Identify the preparation type.
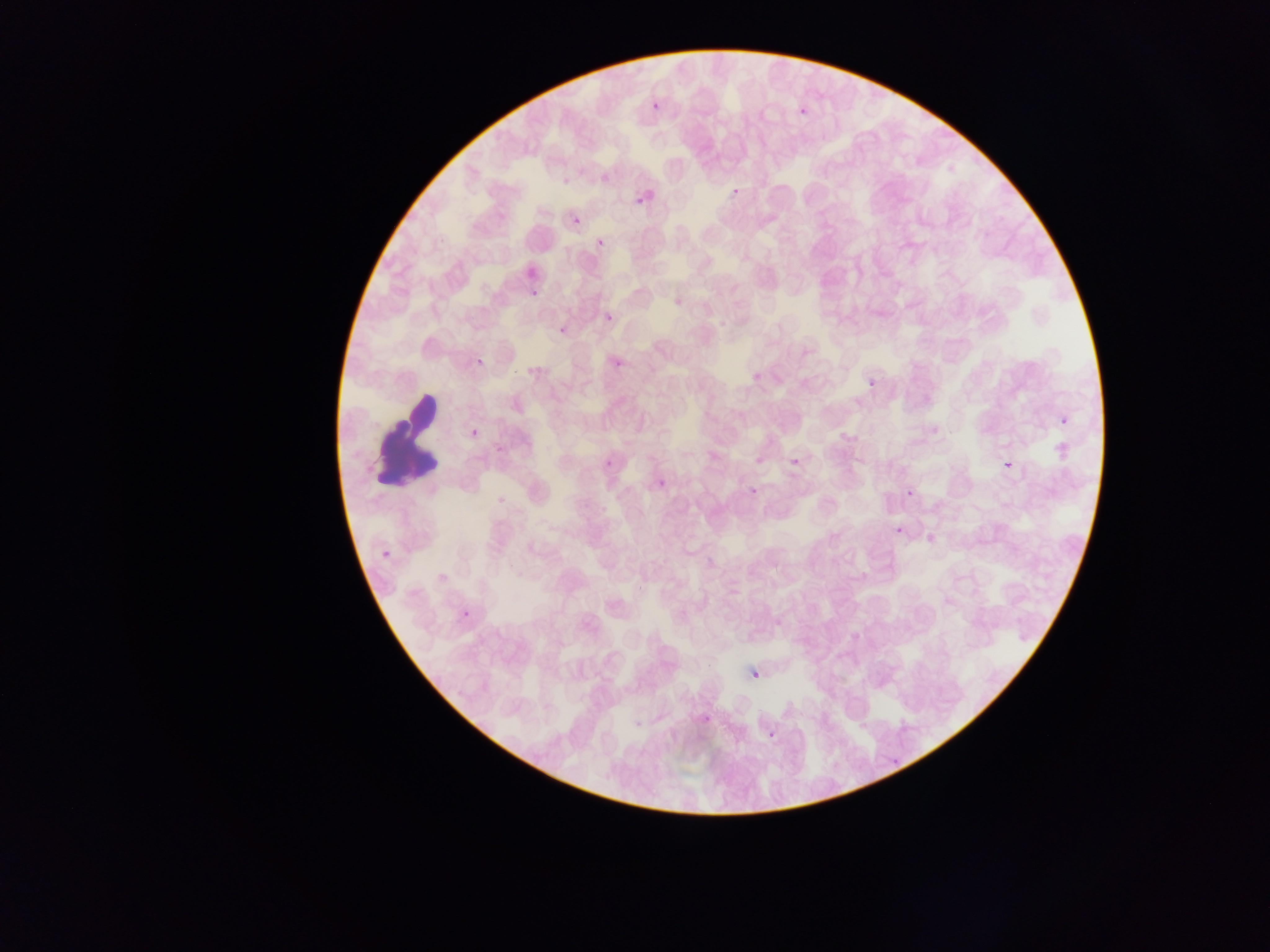

This is a thin smear.

country = Ghana
image size = 1270×952 pixels
malaria parasite locations = approximate bounding boxes as {left, top, right, bottom} in pixels: {650, 100, 661, 112}, {797, 105, 811, 121}, {561, 176, 574, 189}, {597, 176, 612, 189}, {730, 186, 743, 200}, {632, 188, 657, 214}, {572, 215, 583, 226}, {596, 238, 607, 250}, {524, 286, 546, 304}, {604, 306, 621, 321}, {604, 312, 616, 325}, {553, 326, 573, 338}, {527, 345, 556, 368}, {612, 356, 627, 372}, {752, 359, 779, 384}, {864, 374, 882, 394}, {1056, 412, 1074, 432}, {466, 425, 483, 443}, {793, 449, 801, 473}, {601, 455, 618, 473}, {1000, 456, 1019, 478}, {753, 460, 767, 466}, {656, 478, 669, 492}, {903, 485, 920, 502}, {748, 487, 758, 498}, {892, 521, 910, 542}, {378, 544, 400, 568}, {457, 605, 478, 627}, {749, 665, 763, 682}, {751, 670, 761, 681}, {767, 729, 776, 739}
field of view = single
leukocyte locations = approximate bounding boxes as {left, top, right, bottom} in pixels: {367, 388, 442, 492}
capture = mobile-phone photograph through a microscope